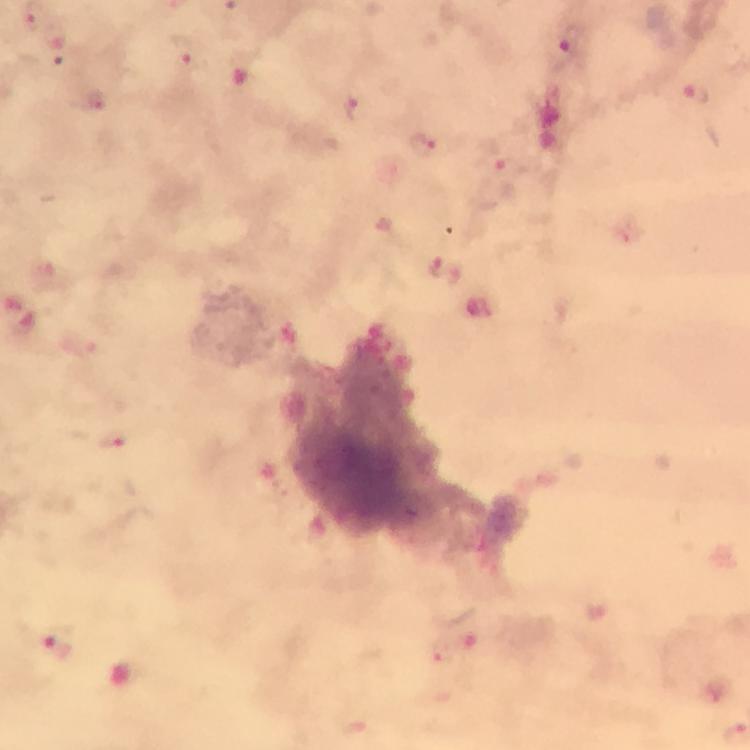

Approximate centers as [x, y] in pixels.
Summary:
  - Plasmodium parasite locations: [52, 39], [561, 49], [185, 54], [694, 96], [95, 100], [354, 108], [424, 145], [493, 159], [434, 265], [453, 275], [115, 442], [467, 632], [54, 644], [441, 656], [356, 723]
  - Image size: 750×750 pixels
  - Capture: smartphone camera through the microscope
  - Magnification: 100x
  - Preparation: thick blood smear
  - Cropped from: a single field of view
  - Context: from a malaria diagnostic workup
  - Stain: Giemsa
  - Immersion oil: applied